Give the position of each P. falciparum parasite with its life-cycle stage, each leukocyte, and any debris.
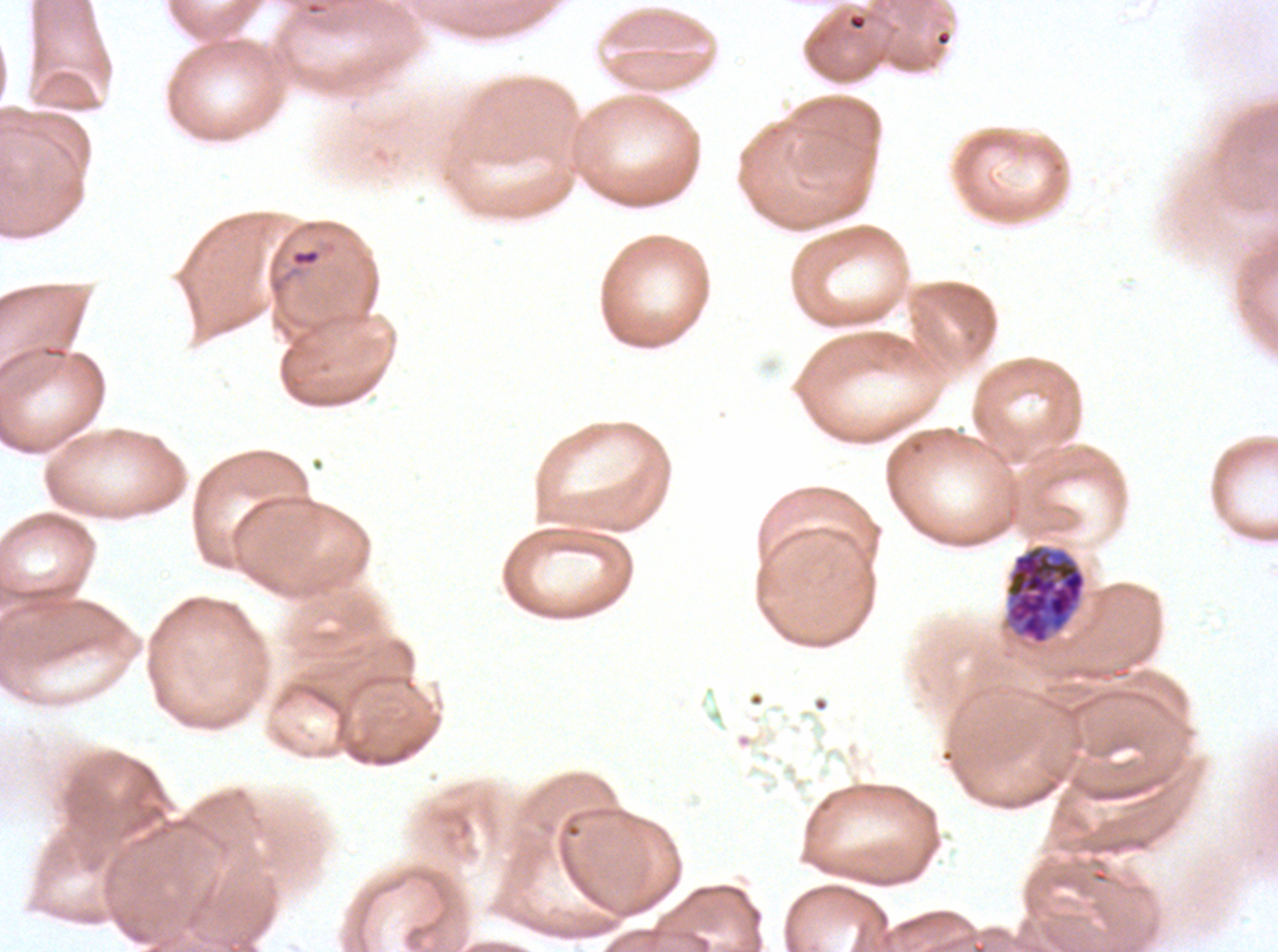

Approximate bounding rectangles given as corner coordinates in pixels from the top-left.
Rings: (x1=291, y1=249, x2=320, y2=265).
Early schizonts: (x1=1005, y1=545, x2=1087, y2=644).
No late-ring/early-trophozoite forms, mid trophozoites, late trophozoites, late schizonts, segmenters, gametocytes, leukocytes, or debris observed.

Thin blood smear. Image is 1278×952 pixels. Life-cycle stages observed: ring, early schizont. Giemsa-stained preparation. P. falciparum from a patient in The Gambia, cultured ex vivo for 24 to 48 hours. One sub-image of a larger composite.